State which parasite is depicted.
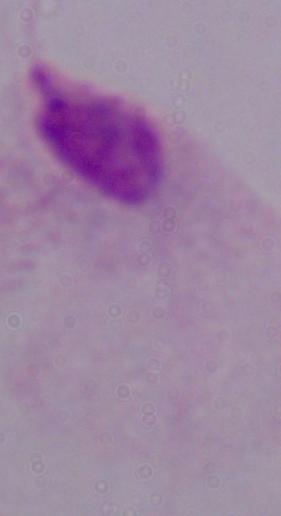

A trichomonad.

Photomicrograph. Captured at 1000x magnification.